Locate every blood parasite and identify its species.
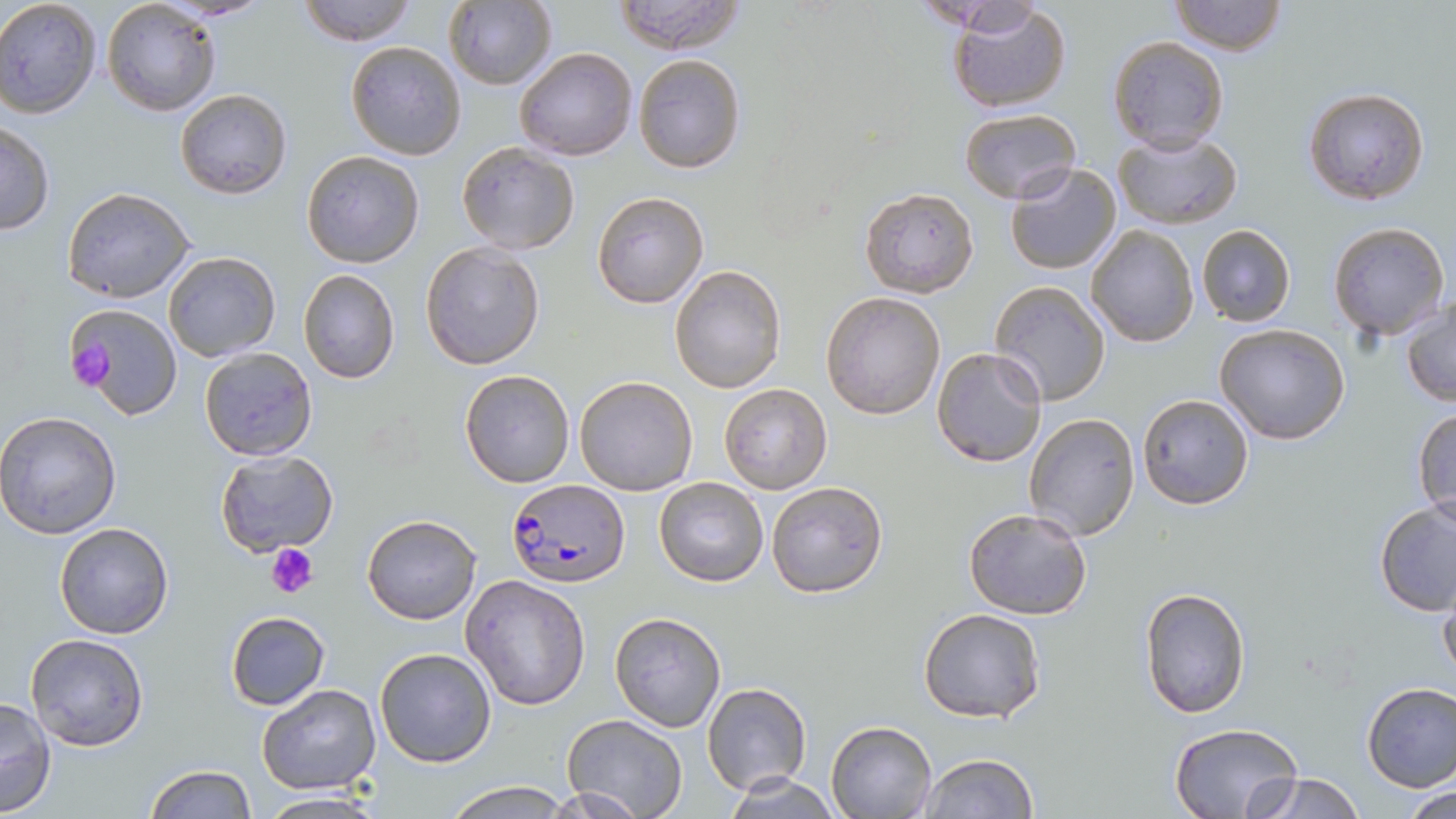

Approximate bounding boxes as [x1, y1, x2, y2] in pixels.
Plasmodium falciparum-infected red blood cells: [506, 477, 628, 586].
No Plasmodium ovale, Plasmodium malariae, Plasmodium vivax, Babesia divergens, or Trypanosoma brucei observed.

slide_level_diagnosis: Plasmodium falciparum
magnification: 1000x
preparation: thin blood smear
uninfected_red_blood_cell_locations: 'approximate bounding boxes as [x1, y1, x2, y2] in pixels: [0, 0, 102, 118], [101, 0, 221, 117], [298, 0, 419, 46], [612, 0, 748, 53], [914, 0, 1047, 32], [1170, 0, 1287, 55], [443, 1, 558, 91], [948, 2, 1073, 114], [1107, 35, 1229, 154], [346, 41, 467, 160], [515, 47, 638, 162], [631, 53, 745, 175], [1303, 86, 1431, 206], [175, 88, 291, 200], [958, 110, 1079, 202], [1, 121, 55, 236], [1113, 130, 1241, 229], [455, 142, 581, 255], [301, 150, 425, 268], [1004, 163, 1122, 275], [63, 186, 196, 303], [859, 186, 980, 297], [591, 192, 710, 309], [1327, 221, 1450, 339], [1195, 223, 1296, 326], [1086, 225, 1198, 348], [420, 242, 544, 370], [164, 251, 281, 362], [670, 263, 786, 394], [298, 269, 401, 384], [989, 282, 1112, 406], [821, 292, 946, 421], [1401, 298, 1456, 406], [63, 303, 183, 422], [1214, 324, 1351, 444], [932, 346, 1048, 466], [199, 347, 318, 461], [458, 369, 575, 488], [573, 376, 698, 496], [720, 383, 831, 493], [1136, 392, 1255, 511], [1412, 403, 1456, 523], [0, 411, 123, 538], [1023, 412, 1140, 541], [214, 451, 339, 557], [654, 477, 768, 586], [766, 481, 890, 599], [1375, 501, 1456, 618], [962, 507, 1094, 621], [363, 514, 481, 624], [54, 522, 174, 640], [461, 573, 592, 710], [1437, 579, 1456, 689], [1138, 586, 1250, 718], [918, 607, 1047, 724], [225, 610, 330, 710], [609, 612, 726, 731], [26, 634, 147, 752], [373, 646, 497, 767], [1360, 682, 1456, 792], [701, 683, 812, 795], [256, 684, 382, 796], [0, 696, 57, 817], [562, 714, 689, 819], [826, 719, 938, 819], [1169, 722, 1302, 819], [917, 753, 1038, 819], [144, 764, 254, 819], [1243, 771, 1364, 819], [724, 774, 843, 817], [443, 780, 571, 818], [1399, 783, 1456, 818], [257, 793, 387, 818]'
field_of_view: single
modality: optical microscopy
platelet_locations: 'approximate bounding boxes as [x1, y1, x2, y2] in pixels: [65, 339, 118, 390], [265, 545, 318, 600]'
stain: May-Grünwald-Giemsa
image_size: 1456×819 pixels